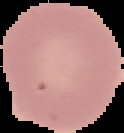
{
  "preparation": "thin blood film",
  "result": "no malaria parasites detected",
  "image_type": "segmented cell region on a black background",
  "image_size": "124×133 pixels"
}